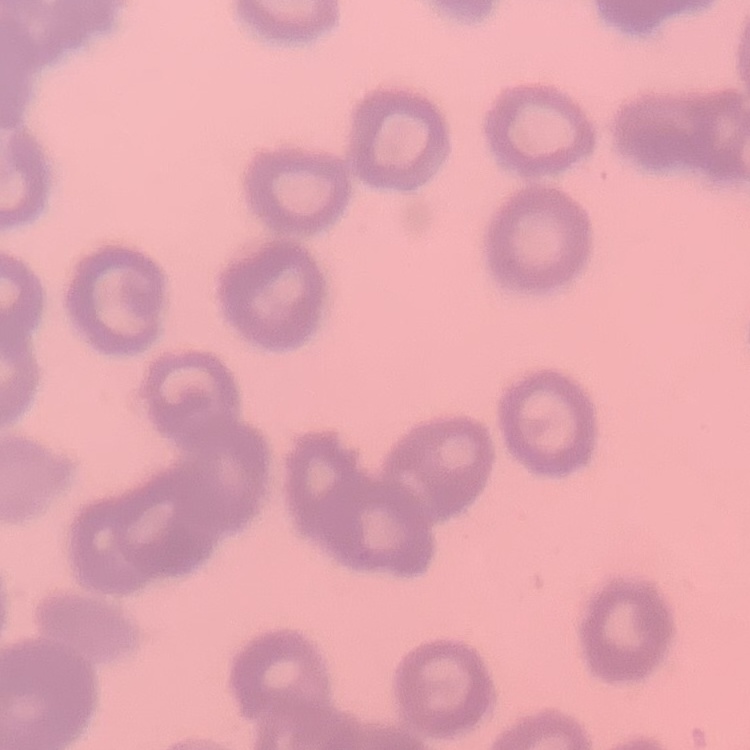
erythrocyte morphology = rouleaux formation
image type = one tile cut from a larger photomicrograph
stain = Field's or Giemsa
preparation = thin blood film